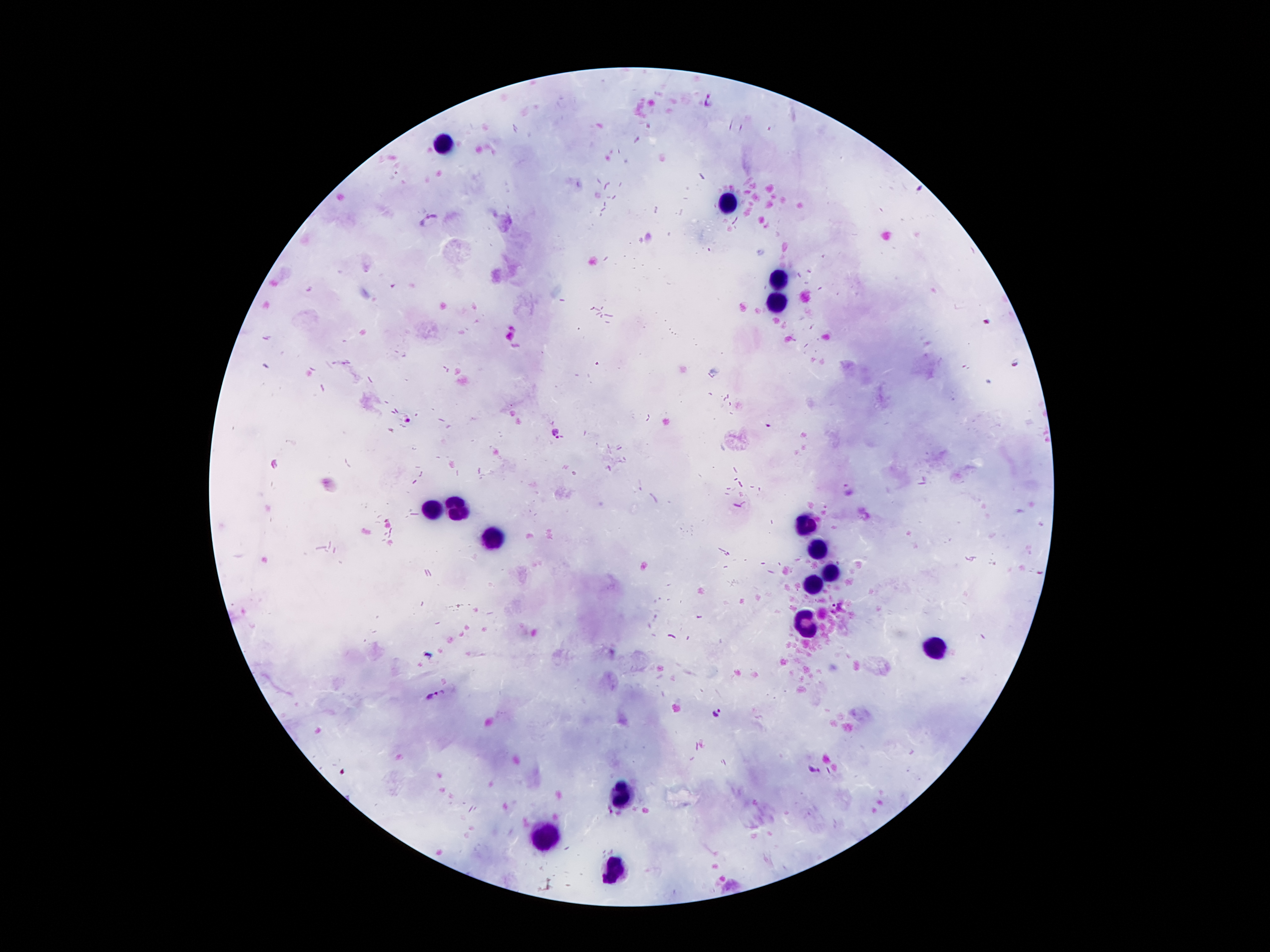
coordinate format = approximate centers as (x, y) in pixels
Plasmodium parasite locations = (709, 99), (428, 219), (986, 321), (1017, 362), (406, 418), (552, 433), (850, 490), (433, 694), (716, 712), (815, 768), (608, 812)
leukocyte locations = (444, 142), (727, 204), (782, 276), (776, 307), (458, 509), (433, 511), (807, 524), (494, 541), (820, 545), (834, 574), (811, 589), (935, 646), (626, 795), (549, 835), (618, 868)
capture = smartphone through the microscope eyepiece
magnification = 100x
stain = Giemsa
image size = 1270×952 pixels
preparation = thick blood smear
patient malaria status = infected with Plasmodium falciparum
field of view = single